Locate every leukocyte (white blood cell).
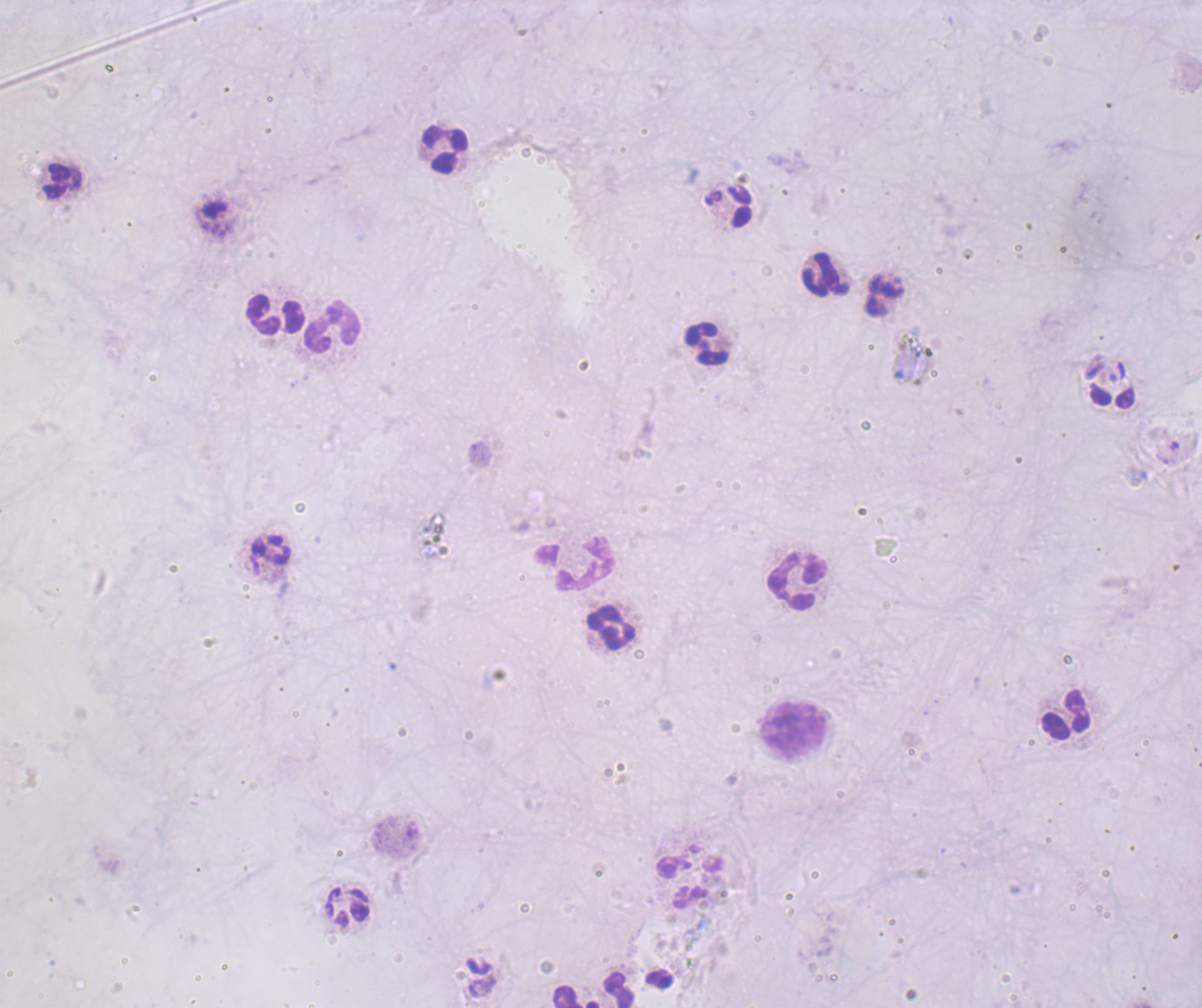
Approximate object centers, in pixels from the top-left corner.
Leukocytes: (x=444, y=150), (x=62, y=181), (x=738, y=206), (x=825, y=274), (x=277, y=315), (x=332, y=326), (x=706, y=343), (x=1111, y=396), (x=573, y=564), (x=796, y=582), (x=610, y=628), (x=1066, y=714), (x=792, y=728), (x=348, y=907), (x=619, y=989), (x=576, y=996).

Thick blood smear. Single field of view. Previously used in a real diagnosis. 100x magnification. Image is 1202×1008 pixels. Result: negative for Plasmodium parasites. Coloration quality: bad. Background quality: poor. Romanowsky stain.